Outline each Plasmodium malariae-infected red blood cell.
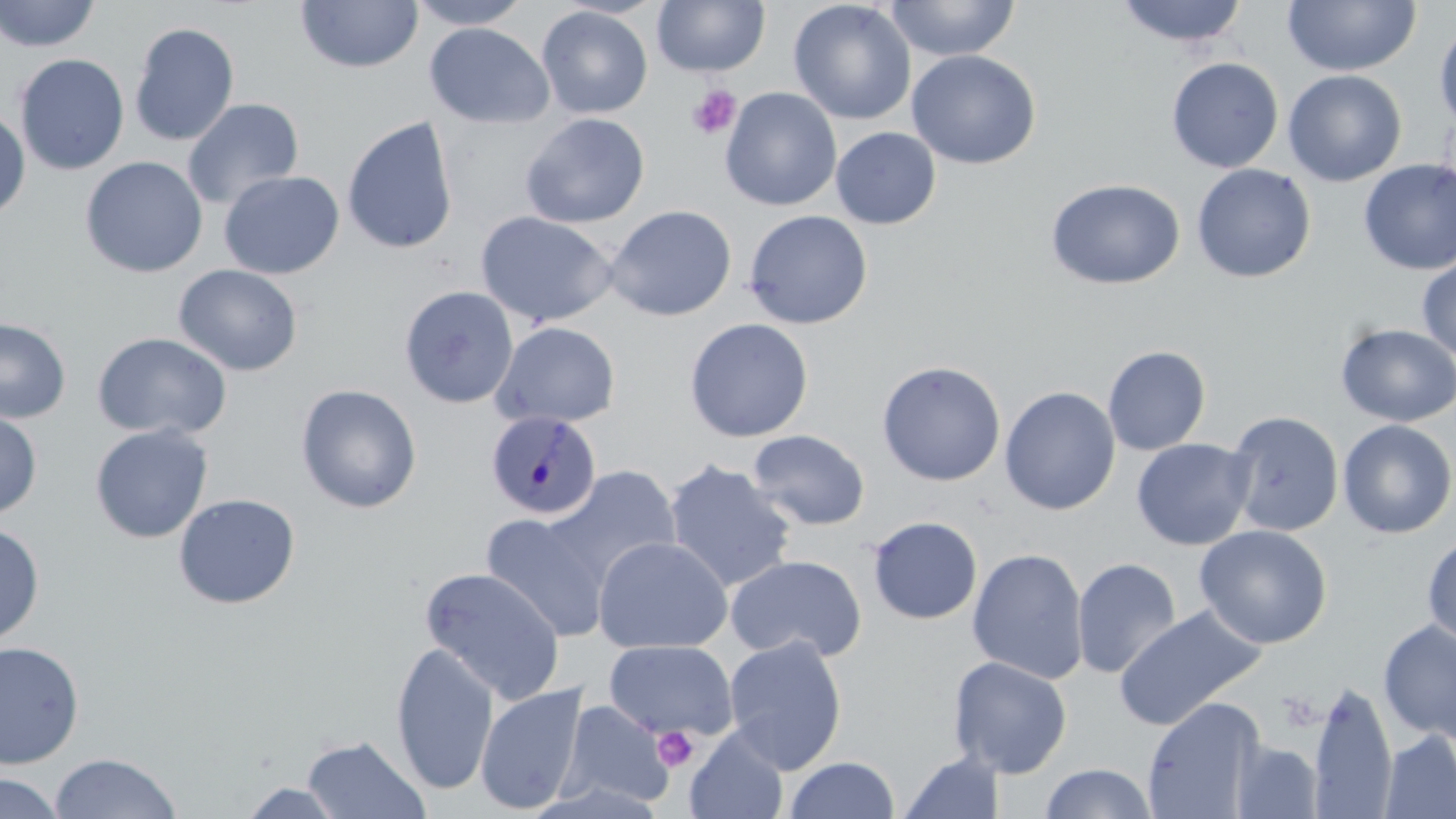
Approximate bounding boxes as (x1, y1, x2, y2) in pixels.
Plasmodium malariae-infected red blood cells: (485, 409, 601, 520).

Summary:
  - Platelet locations: (687, 86, 741, 140), (652, 726, 699, 772)
  - Uninfected red blood cell locations: (0, 0, 101, 52), (406, 0, 534, 30), (652, 0, 770, 77), (884, 0, 1021, 61), (1114, 0, 1249, 48), (1282, 0, 1420, 77), (295, 1, 424, 73), (788, 1, 917, 125), (536, 5, 653, 119), (1434, 19, 1456, 134), (129, 22, 240, 147), (424, 23, 555, 129), (906, 49, 1041, 170), (14, 53, 130, 176), (1166, 57, 1284, 173), (1283, 69, 1407, 187), (719, 86, 842, 212), (182, 97, 304, 210), (0, 108, 31, 220), (520, 112, 650, 229), (341, 115, 459, 255), (830, 126, 941, 230), (80, 156, 208, 278), (1358, 158, 1456, 275), (1191, 163, 1316, 283), (218, 170, 344, 280), (1046, 178, 1185, 290), (605, 204, 738, 321), (743, 209, 874, 329), (475, 210, 620, 327), (1416, 255, 1456, 362), (173, 264, 303, 376), (399, 285, 520, 409), (0, 317, 71, 424), (683, 317, 814, 443), (490, 321, 622, 429), (1336, 323, 1456, 427), (92, 332, 231, 441), (1102, 345, 1211, 455), (876, 360, 1007, 486), (296, 384, 422, 513), (999, 385, 1121, 515), (0, 409, 42, 520), (1226, 410, 1344, 537), (1337, 419, 1455, 540), (89, 424, 213, 544), (748, 429, 871, 531), (1131, 437, 1256, 551), (663, 459, 798, 593), (541, 465, 682, 592), (173, 493, 300, 610), (479, 511, 612, 642), (866, 515, 983, 625), (0, 521, 45, 648), (1194, 524, 1332, 649), (1422, 534, 1456, 647), (592, 536, 733, 654), (967, 548, 1089, 684), (725, 554, 867, 663), (1072, 557, 1182, 679), (419, 566, 566, 705), (1113, 605, 1267, 732), (1378, 620, 1456, 742), (723, 636, 848, 774), (603, 639, 738, 741), (0, 641, 84, 769), (390, 641, 500, 795), (948, 656, 1073, 778), (475, 682, 589, 815), (1309, 683, 1397, 819), (1142, 697, 1265, 819), (556, 699, 675, 810), (685, 727, 789, 819), (1379, 730, 1456, 819), (300, 734, 430, 818), (1232, 740, 1323, 818), (898, 751, 1006, 819), (49, 752, 183, 818), (783, 756, 900, 818), (1039, 763, 1158, 819), (0, 772, 66, 819), (237, 781, 350, 818)
  - Slide-level diagnosis: Plasmodium malariae
  - Magnification: 1000x
  - Field of view: single
  - Preparation: thin blood smear
  - Modality: optical microscopy
  - Image size: 1456×819 pixels
  - Stain: May-Grünwald-Giemsa